Report the malaria status of this cell.
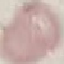
Uninfected.

Thin smear of blood. Giemsa stain. Acquired by smartphone through the microscope eyepiece. Cell patch, automatically extracted from a larger field of view and resized to 64 × 64 pixels.